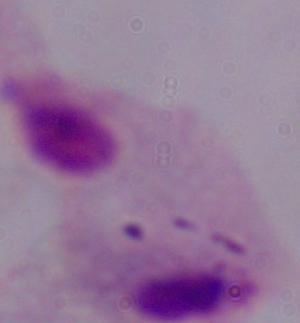
Summary:
  - Identification: trichomonad
  - Magnification: 1000x
  - Modality: photomicrograph